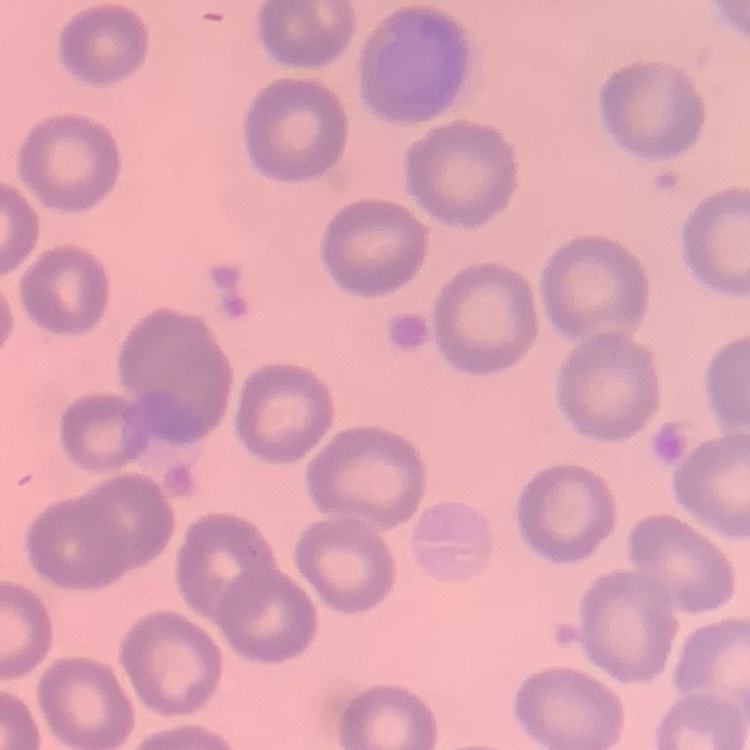

The erythrocytes show no rouleaux formation. One tile cut from a larger photomicrograph. Thin blood film. Stained with either Field's or Giemsa.